Locate every Plasmodium parasite and every leukocyte.
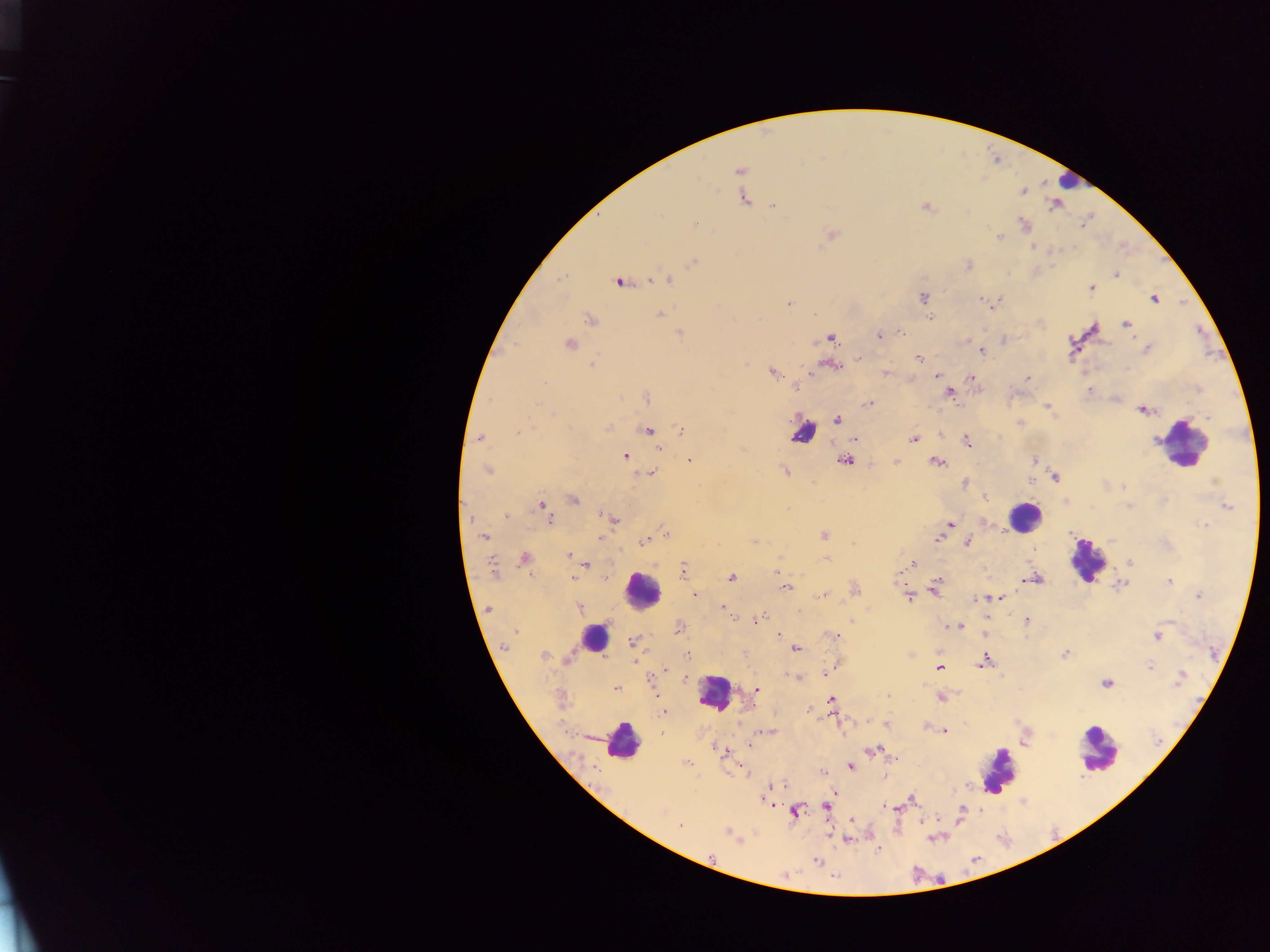
Approximate centers as [x, y] in pixels.
Plasmodium parasites: [739, 170], [1023, 191], [744, 199], [774, 206], [926, 207], [696, 222], [1024, 224], [831, 233], [999, 236], [1033, 247], [693, 262], [968, 265], [1116, 275], [667, 278], [653, 279], [618, 282], [1091, 288], [923, 297], [981, 299], [1155, 299], [788, 303], [660, 314], [931, 318], [591, 320], [1126, 323], [680, 333], [902, 333], [880, 335], [830, 338], [1004, 340], [569, 344], [1146, 348], [982, 351], [860, 358], [918, 359], [592, 365], [834, 366], [773, 372], [885, 372], [937, 375], [970, 378], [1028, 378], [796, 388], [1088, 390], [950, 393], [647, 398], [869, 403], [1048, 406], [1144, 410], [837, 420], [1019, 423], [606, 429], [682, 430], [648, 431], [518, 433], [480, 437], [855, 438], [913, 438], [966, 442], [659, 448], [625, 456], [689, 460], [1034, 460], [844, 462], [896, 462], [936, 462], [487, 470], [785, 471], [651, 473], [1055, 478], [1031, 480], [965, 483], [1123, 487], [985, 498], [573, 500], [541, 505], [1227, 506], [506, 516], [550, 519], [614, 519], [949, 524], [1205, 525], [666, 532], [824, 535], [484, 537], [600, 539], [937, 539], [645, 541], [754, 541], [967, 543], [568, 556], [524, 558], [826, 559], [1130, 562], [913, 564], [586, 565], [492, 567], [683, 571], [900, 572], [573, 578], [731, 578], [1034, 579], [938, 581], [1169, 581], [1121, 584], [786, 587], [935, 590], [823, 595], [908, 595], [695, 596], [1198, 596], [999, 598], [980, 599], [975, 600], [722, 606], [579, 608], [489, 609], [725, 611], [762, 615], [733, 618], [1027, 621], [852, 622], [957, 626], [679, 629], [515, 632], [778, 635], [833, 636], [1158, 636], [632, 642], [506, 646], [796, 649], [1065, 653], [688, 655], [544, 656], [568, 658], [984, 662], [1150, 666], [939, 667], [664, 671], [831, 671], [826, 673], [797, 678], [1180, 678], [685, 679], [1106, 684], [615, 688], [756, 690], [941, 698], [832, 701], [664, 711], [887, 724], [943, 731], [768, 732], [750, 745], [872, 750], [723, 752], [686, 763], [851, 767], [780, 786], [912, 800], [826, 806], [887, 808], [796, 811], [680, 826], [728, 834], [846, 839], [817, 861].
Leukocytes: [1067, 181], [802, 433], [1181, 442], [1024, 516], [1087, 560], [642, 590], [594, 639], [714, 692], [622, 741], [1098, 750], [998, 770].

Summary:
  - Capture: mobile-phone photograph through a microscope
  - Country: Ghana
  - Image size: 1270×952 pixels
  - Preparation: thick blood smear
  - Field of view: single